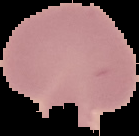

Summary:
  - Image type: segmented cell region with the area outside set to black
  - Result: no Plasmodium parasites seen
  - Image size: 139×136 pixels
  - Preparation: thin blood smear